Describe the morphology of the erythrocytes.
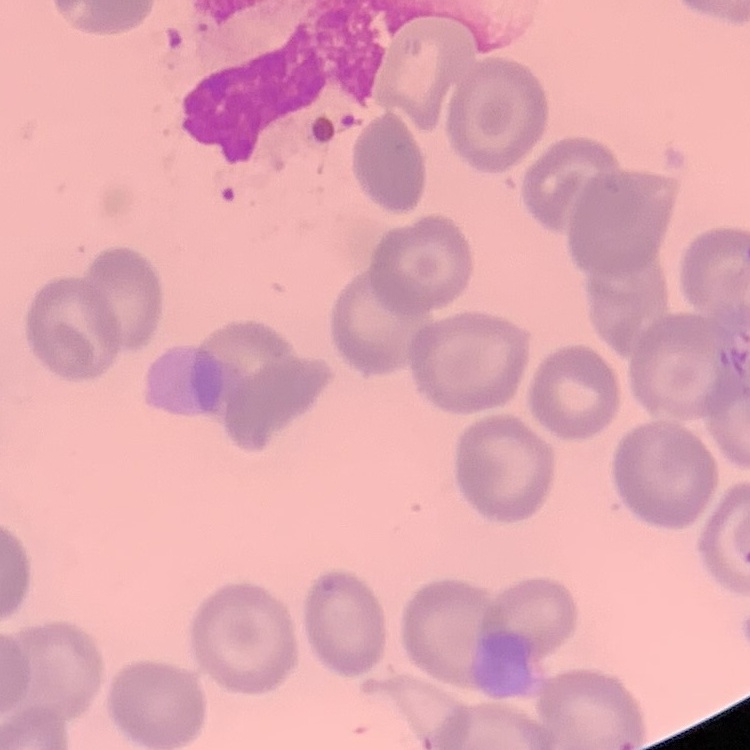
They show no rouleaux formation.

Thin blood film. Square crop of a larger photomicrograph. Field's or Giemsa stain.